Assess this cell for malaria.
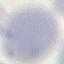
Uninfected.

Acquired by smartphone through the microscope eyepiece. Automatically extracted cell patch, resized to 64 × 64 pixels. Giemsa-stained preparation. Thin blood film.